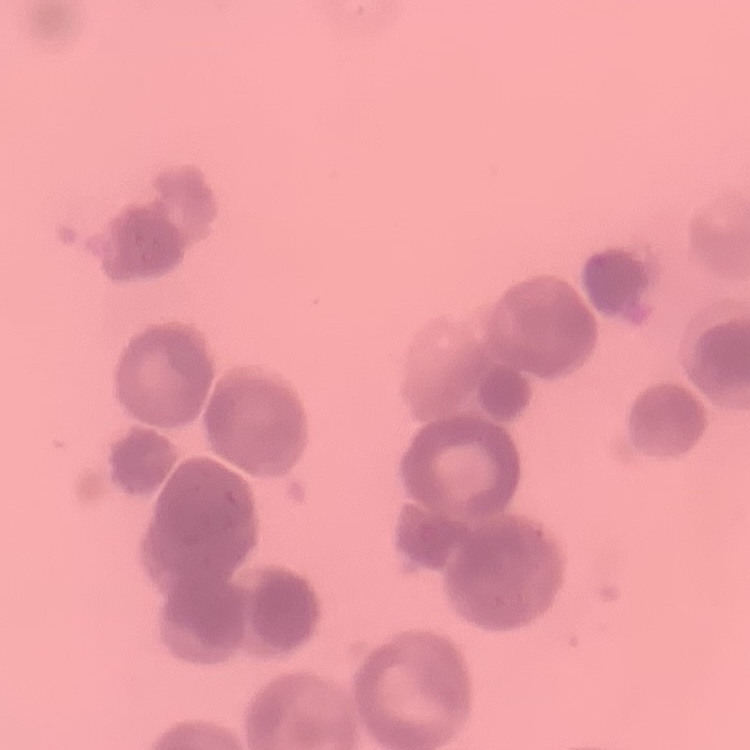

red blood cell morphology = rouleaux formation
stain = Field's or Giemsa
image type = square crop of a larger photomicrograph
preparation = thin blood film